Assess this cell for malaria.
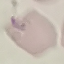

Parasitized.

{
  "capture": "smartphone camera at the microscope eyepiece",
  "image_type": "cell patch, automatically extracted from a larger field of view and resized to 64 × 64 pixels",
  "stain": "Giemsa",
  "preparation": "thin smear"
}